Describe the morphology of the erythrocytes.
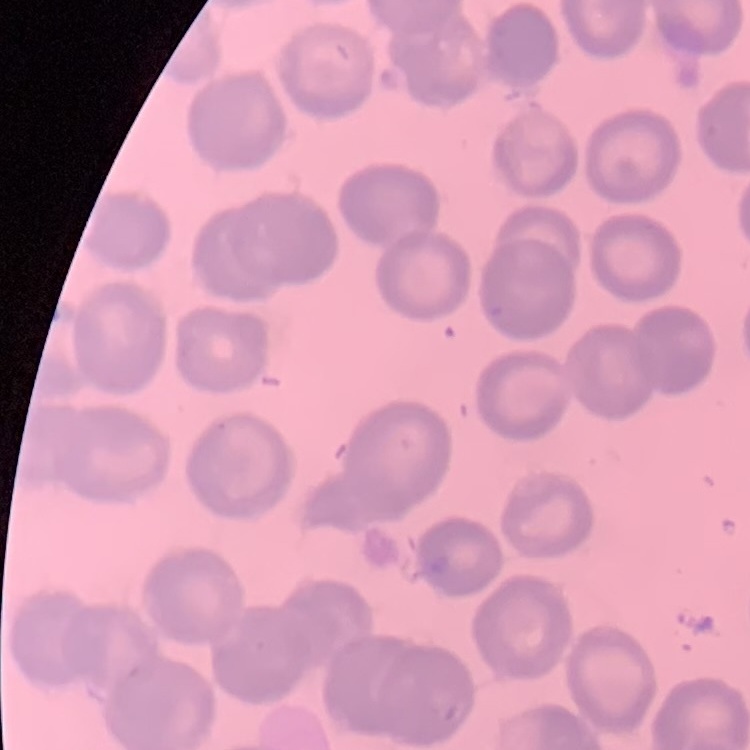
No rouleaux formation.

preparation = thin peripheral smear
image type = square crop of a larger photomicrograph
stain = Field's or Giemsa